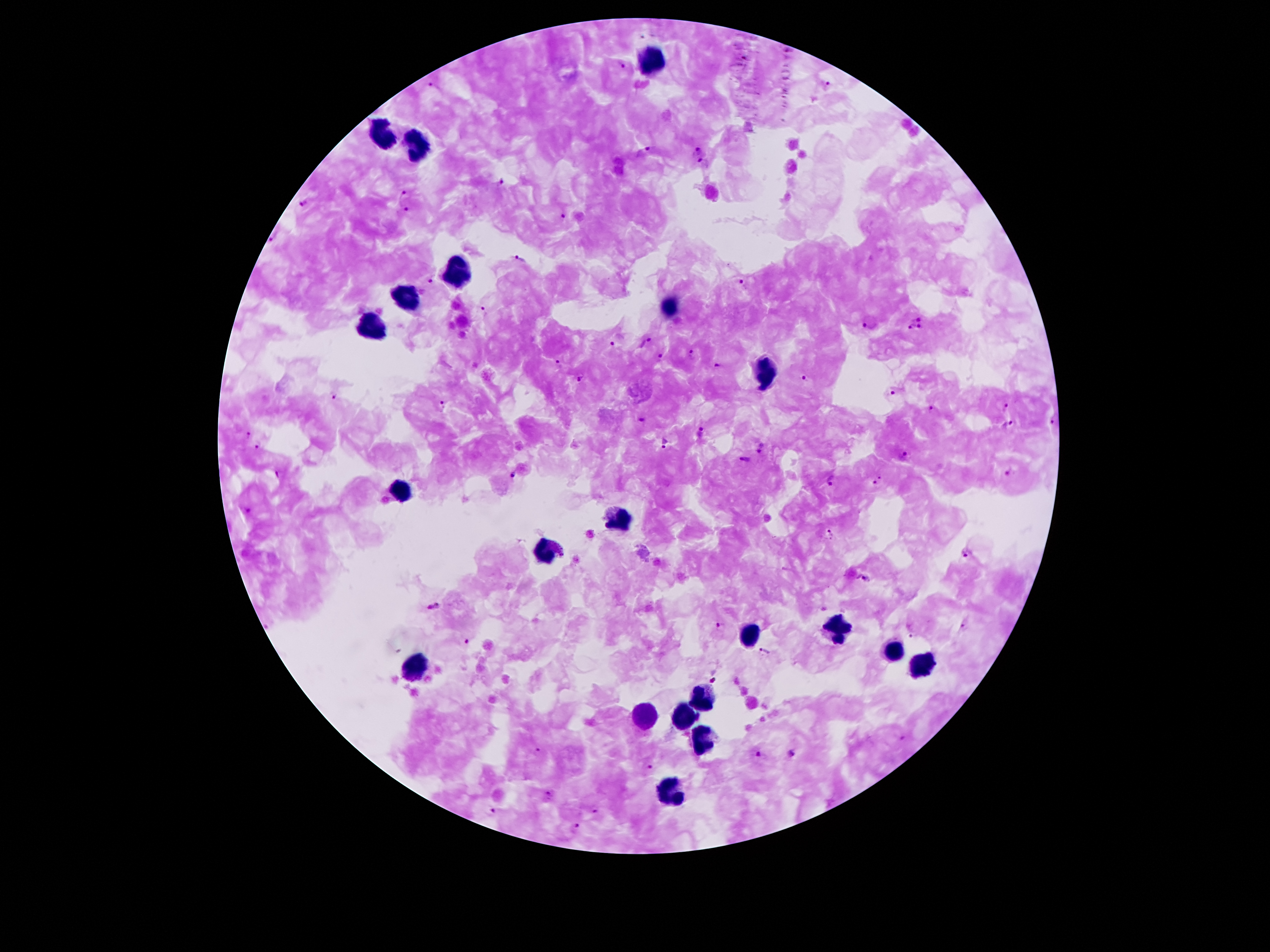

coordinate format = approximate object centers, in pixels from the top-left corner
Plasmodium parasite locations = (x=622, y=65), (x=828, y=84), (x=431, y=85), (x=697, y=151), (x=643, y=152), (x=701, y=161), (x=501, y=182), (x=405, y=192), (x=302, y=202), (x=407, y=208), (x=561, y=216), (x=270, y=238), (x=519, y=258), (x=428, y=280), (x=742, y=283), (x=489, y=312), (x=917, y=318), (x=867, y=323), (x=910, y=326), (x=920, y=326), (x=612, y=342), (x=647, y=342), (x=660, y=354), (x=692, y=354), (x=559, y=362), (x=719, y=365), (x=581, y=377), (x=804, y=379), (x=890, y=391), (x=332, y=397), (x=443, y=406), (x=931, y=408), (x=1006, y=408), (x=641, y=421), (x=1051, y=422), (x=1007, y=424), (x=701, y=431), (x=247, y=433), (x=256, y=444), (x=665, y=444), (x=760, y=447), (x=902, y=454), (x=744, y=458), (x=1008, y=471), (x=279, y=472), (x=511, y=476), (x=831, y=481), (x=880, y=481), (x=248, y=510), (x=829, y=534), (x=967, y=553), (x=864, y=578), (x=434, y=605), (x=720, y=624), (x=963, y=628), (x=911, y=634), (x=467, y=641), (x=764, y=650), (x=713, y=680), (x=901, y=738), (x=536, y=750), (x=792, y=753), (x=758, y=754), (x=649, y=766), (x=548, y=794), (x=593, y=811), (x=493, y=812), (x=576, y=827)
leukocyte locations = (x=655, y=60), (x=381, y=133), (x=417, y=147), (x=461, y=270), (x=408, y=297), (x=669, y=308), (x=368, y=326), (x=762, y=374), (x=399, y=489), (x=620, y=518), (x=545, y=551), (x=837, y=629), (x=748, y=633), (x=892, y=653), (x=414, y=666), (x=921, y=666), (x=702, y=697), (x=684, y=713), (x=642, y=719), (x=704, y=743), (x=671, y=794)
capture = smartphone camera through the microscope eyepiece
image size = 1270×952 pixels
stain = Giemsa
magnification = 100x
preparation = thick blood film
patient malaria status = positive for Plasmodium falciparum
field of view = single